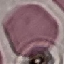 Result: no malaria parasites detected. Cell patch, automatically extracted from a larger field of view and resized to 64 × 64 pixels. Photographed with a smartphone camera at the microscope eyepiece. Thin blood smear. Giemsa stain.